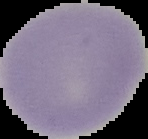

From a thin blood smear. Image is 148×139 pixels. Malaria status: uninfected. Segmented cell region on a black background.